Name the cell type shown.
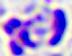

This is a leukocyte.

Summary:
  - Modality: micrograph
  - Magnification: 400x